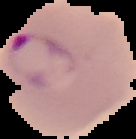
From a thin blood smear. Image is 136×139 pixels. Segmented cell region on a black background. Result: Plasmodium parasites identified.